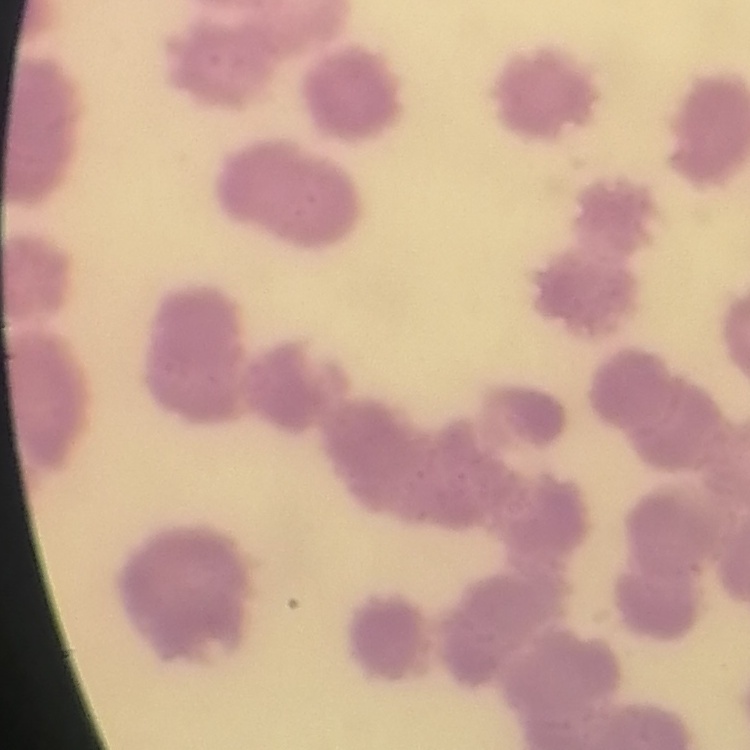

erythrocyte morphology = rouleaux formation
image type = one tile cut from a larger photomicrograph
preparation = thin blood smear
stain = Field's or Giemsa